Locate every blood parasite and identify its species.
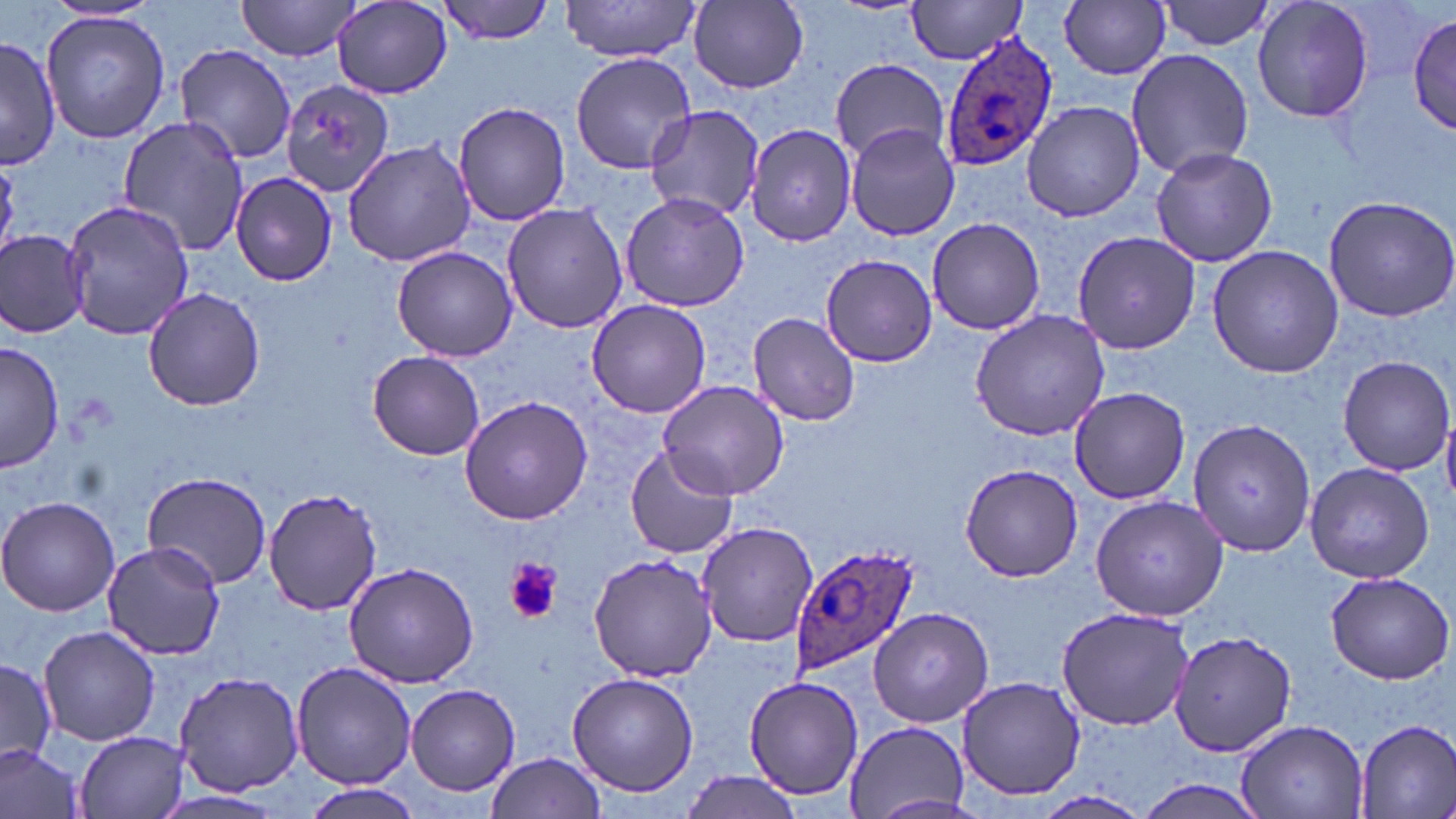
Approximate bounding boxes as (x1,y1)-(x2,y2) corner pairs in pixels.
Plasmodium ovale-infected red blood cells: (937,29)-(1060,173), (789,541)-(919,675).
No Plasmodium falciparum, Plasmodium malariae, Plasmodium vivax, Babesia divergens, or Trypanosoma brucei observed.

slide-level diagnosis = Plasmodium ovale
preparation = thin blood film
field of view = single
uninfected red blood cell locations = approximate bounding boxes as (x1,y1)-(x2,y2) corner pairs in pixels: (236,0)-(364,60), (436,0)-(557,44), (560,0)-(701,61), (906,0)-(1028,63), (1158,0)-(1277,52), (1251,0)-(1377,123), (332,1)-(453,98), (688,1)-(810,91), (1060,2)-(1171,79), (39,10)-(170,144), (1410,13)-(1455,139), (1,36)-(59,168), (174,43)-(297,166), (1126,49)-(1254,178), (570,51)-(697,175), (831,58)-(950,164), (273,74)-(390,199), (1021,100)-(1144,222), (452,101)-(573,226), (646,105)-(767,219), (119,116)-(250,256), (843,123)-(959,241), (746,124)-(858,245), (341,138)-(477,266), (1149,144)-(1280,267), (230,172)-(339,287), (620,191)-(748,312), (1322,192)-(1456,322), (63,198)-(194,342), (502,204)-(628,336), (926,217)-(1047,335), (0,231)-(90,337), (1072,231)-(1204,354), (1206,245)-(1345,379), (392,246)-(517,361), (819,254)-(938,367), (141,287)-(268,410), (586,300)-(713,419), (970,310)-(1110,442), (747,311)-(861,426), (1,342)-(65,473), (367,350)-(485,460), (1336,354)-(1455,476), (656,380)-(789,500), (1066,388)-(1192,504), (459,396)-(592,525), (1442,407)-(1456,507), (1187,418)-(1314,557), (625,444)-(739,560), (1303,462)-(1434,583), (958,463)-(1087,582), (143,470)-(273,589), (263,486)-(384,615), (1088,496)-(1227,621), (0,497)-(121,617), (696,521)-(818,646), (101,541)-(226,659), (588,553)-(720,682), (342,560)-(480,686), (1324,572)-(1454,684), (1056,605)-(1194,731), (868,607)-(993,727), (37,626)-(162,748), (1169,630)-(1296,757), (0,659)-(57,766), (292,662)-(414,788), (173,669)-(306,796), (567,672)-(699,796), (742,673)-(864,802), (954,675)-(1086,803), (406,683)-(520,797), (1235,717)-(1369,819), (1351,717)-(1456,819), (841,722)-(969,815), (75,731)-(189,818), (0,744)-(86,819), (485,752)-(606,819), (678,771)-(807,818), (1132,777)-(1272,819), (302,781)-(423,819), (1034,790)-(1153,819), (155,791)-(284,818)
magnification = 1000x
image size = 1456×819 pixels
modality = light microscopy
platelet locations = approximate bounding boxes as (x1,y1)-(x2,y2) corner pairs in pixels: (507,556)-(561,624)
stain = May-Grünwald-Giemsa